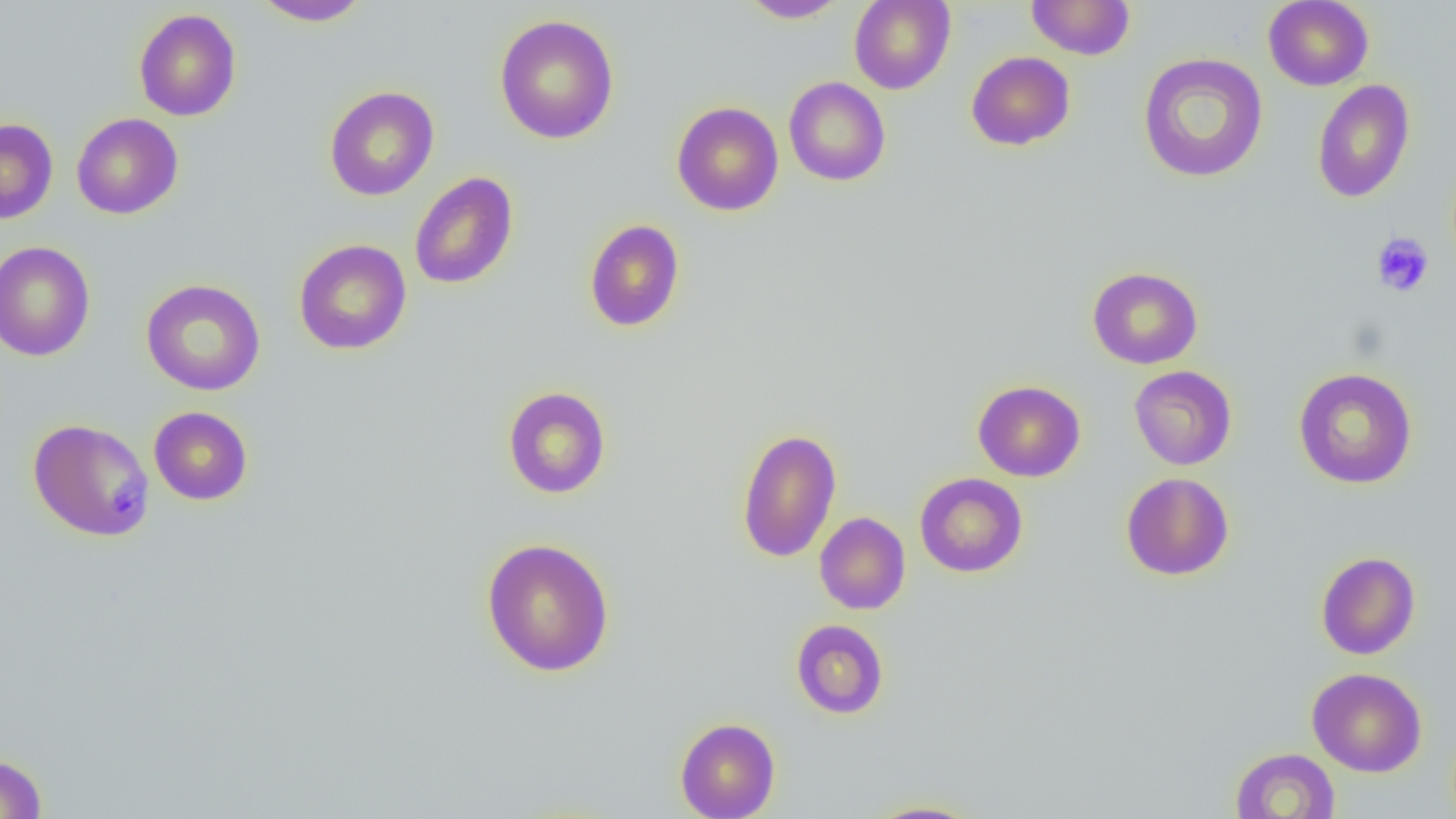
Summary:
  - Coordinate format: approximate bounding boxes as [x1, y1, x2, y2] in pixels
  - Platelet locations: [1371, 232, 1436, 298]
  - Uninfected red blood cell locations: [251, 0, 372, 27], [739, 0, 847, 23], [849, 0, 955, 94], [1026, 0, 1135, 59], [1263, 0, 1374, 91], [133, 8, 241, 121], [494, 14, 619, 144], [966, 51, 1075, 151], [1138, 52, 1268, 183], [783, 76, 891, 186], [1312, 79, 1415, 204], [323, 85, 439, 201], [671, 101, 784, 216], [71, 112, 183, 219], [0, 118, 58, 224], [409, 172, 519, 290], [584, 218, 685, 333], [294, 239, 411, 356], [0, 241, 95, 361], [1087, 267, 1203, 369], [140, 278, 266, 396], [1129, 365, 1237, 470], [1293, 367, 1418, 489], [972, 380, 1086, 482], [502, 386, 612, 499], [148, 406, 253, 505], [27, 418, 155, 543], [736, 428, 842, 563], [1121, 472, 1234, 581], [915, 473, 1028, 577], [814, 512, 910, 614], [481, 537, 616, 677], [1316, 551, 1420, 660], [790, 619, 889, 719], [1306, 667, 1427, 777], [675, 717, 780, 819], [1230, 747, 1340, 819], [0, 753, 48, 818], [863, 799, 985, 818]
  - Slide-level diagnosis: no evidence of blood parasites
  - Image size: 1456×819 pixels
  - Preparation: thin blood film
  - Modality: optical microscopy
  - Magnification: 1000x
  - Field of view: one of a larger specimen